Assess this cell for malaria.
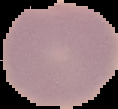

Uninfected.

Cell region segmented out of the field of view; the surrounding area is masked to black. From a thin blood film. Image is 118×109 pixels.